Give the preparation type.
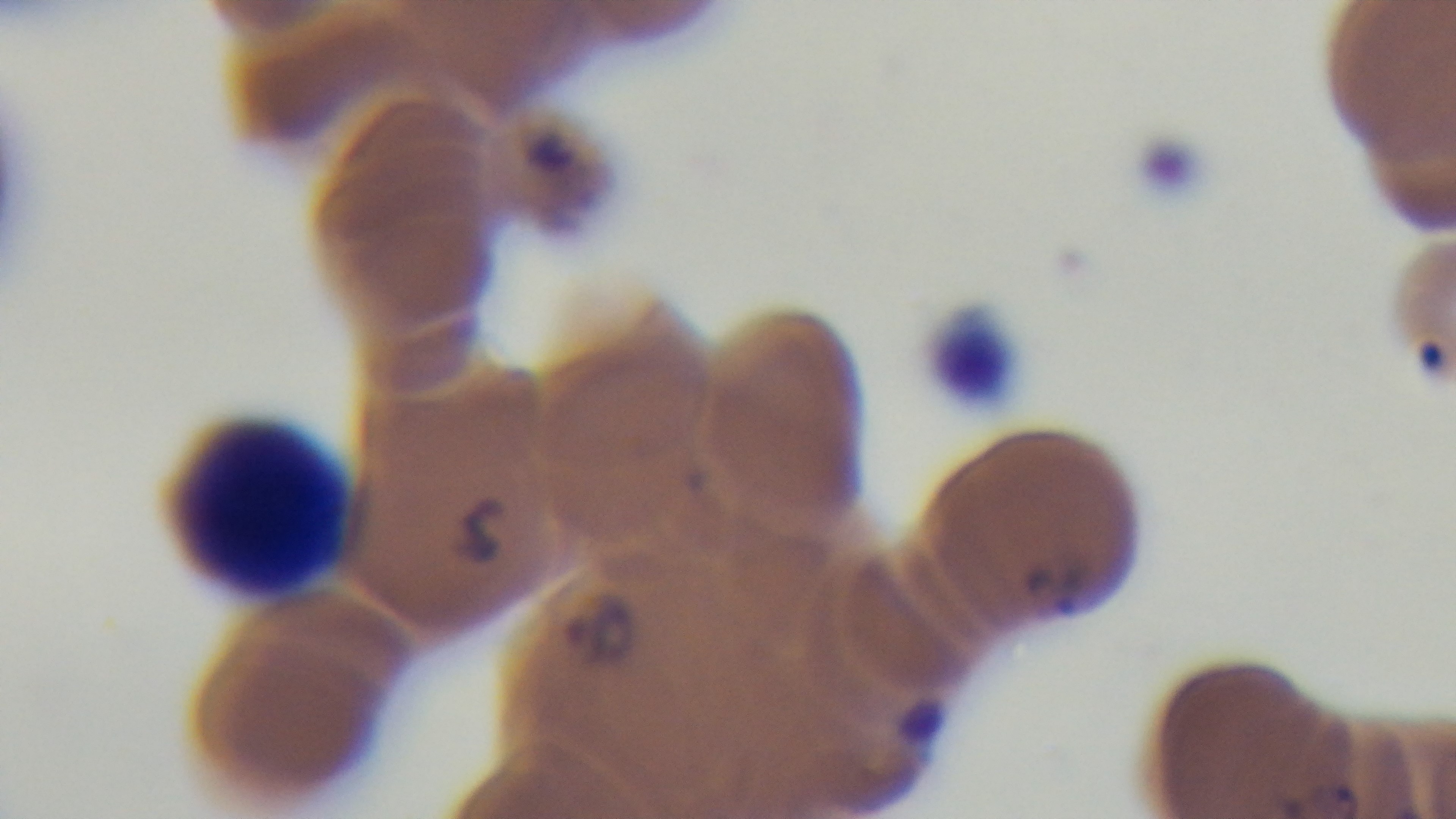
It is a thin blood film.

malaria status = positive
stain = Giemsa
modality = light microscopy
objective = 100x oil immersion
field of view = single
capture = mounted 4K digital camera